Name the parasite shown.
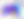

Toxoplasma gondii.

Summary:
  - Modality: photomicrograph
  - Magnification: 400x